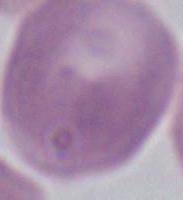
Summary:
  - Modality: photomicrograph
  - Magnification: 1000x
  - Identification: red blood cell